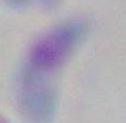
Summary:
  - Magnification: 1000x
  - Identification: Toxoplasma gondii
  - Modality: photomicrograph